Point out each leukocyte.
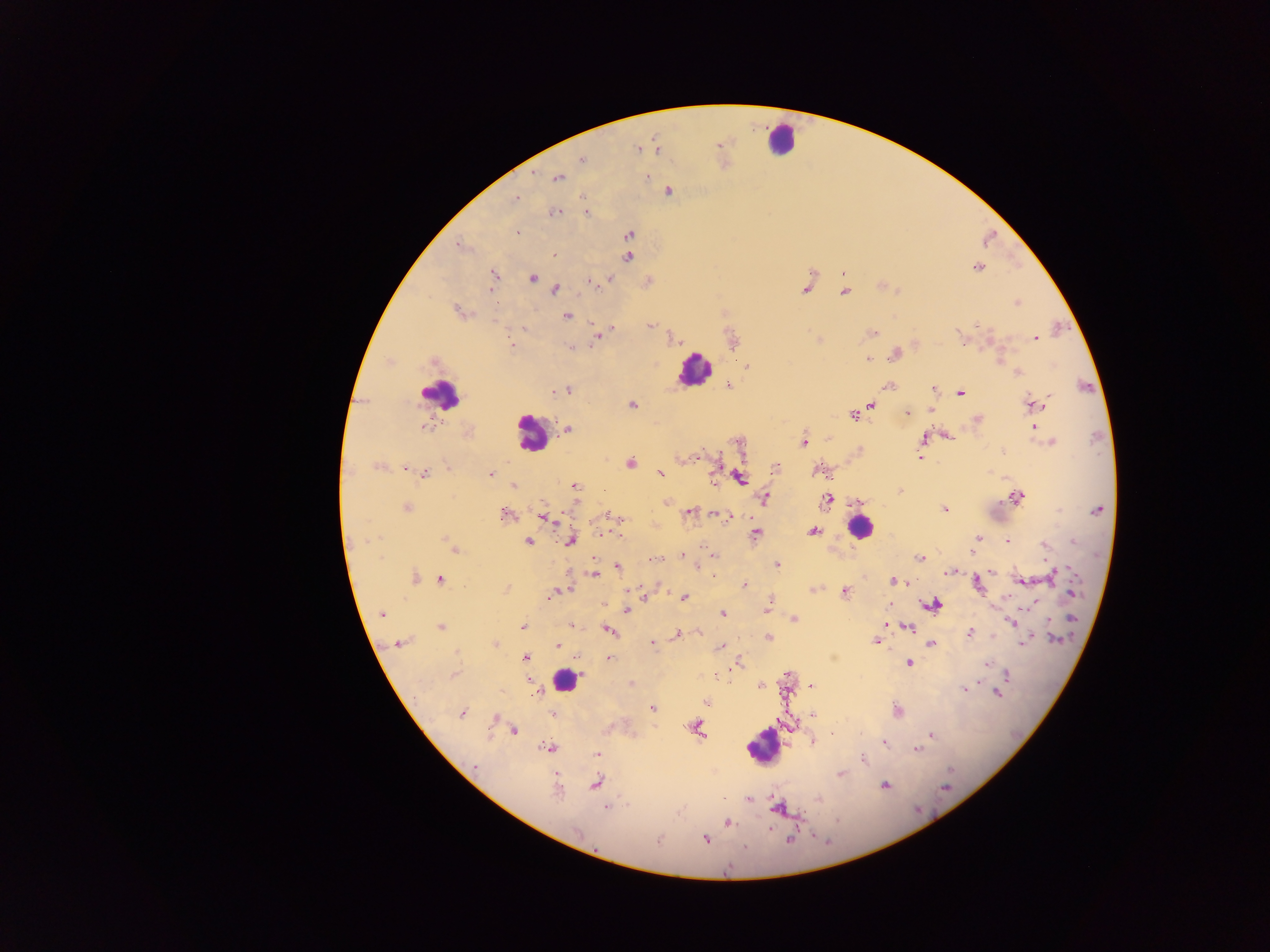

Approximate centers as (x, y) in pixels.
Leukocytes: (780, 139), (695, 371), (441, 395), (531, 433), (859, 527), (564, 676), (762, 746).

Summary:
  - Malaria parasite locations: (638, 149), (657, 149), (582, 160), (646, 176), (557, 177), (668, 191), (516, 198), (554, 212), (586, 212), (517, 232), (629, 234), (459, 246), (554, 256), (628, 257), (978, 267), (844, 273), (494, 275), (532, 278), (608, 279), (594, 282), (555, 289), (806, 289), (490, 290), (845, 292), (1017, 303), (457, 312), (567, 316), (593, 322), (650, 325), (978, 325), (611, 328), (524, 329), (873, 332), (959, 334), (596, 338), (674, 338), (1034, 339), (510, 345), (570, 348), (894, 355), (867, 359), (747, 366), (1018, 373), (728, 386), (888, 387), (934, 389), (567, 390), (556, 391), (960, 393), (872, 404), (1033, 404), (632, 405), (930, 410), (906, 412), (853, 415), (977, 420), (1034, 426), (424, 427), (568, 429), (947, 436), (922, 438), (739, 442), (803, 442), (1051, 442), (1002, 452), (696, 456), (920, 457), (632, 463), (378, 466), (776, 468), (405, 469), (660, 473), (423, 474), (490, 474), (739, 477), (713, 482), (574, 485), (513, 486), (900, 491), (1017, 498), (764, 499), (827, 500), (858, 501), (667, 502), (542, 506), (407, 508), (945, 509), (1097, 510), (690, 513), (505, 515), (606, 515), (718, 515), (543, 516), (727, 517), (619, 518), (812, 531), (756, 533), (977, 539), (570, 541), (1007, 541), (528, 542), (1074, 542), (451, 545), (1044, 546), (454, 548), (973, 551), (681, 554), (715, 556), (920, 557), (652, 560), (777, 565), (618, 566), (948, 572), (991, 572), (595, 574), (1055, 574), (415, 578), (441, 580), (893, 581), (1022, 581), (904, 582), (744, 584), (978, 584), (506, 589), (564, 591), (845, 591), (1071, 592), (552, 594), (645, 597), (684, 598), (602, 604), (890, 604), (933, 604), (627, 610), (766, 611), (382, 614), (723, 614), (1072, 618), (794, 619), (1011, 621), (886, 623), (570, 625), (523, 626), (441, 627), (909, 627), (608, 630), (969, 633), (677, 634), (768, 638), (1056, 640), (876, 641), (1024, 642), (401, 643), (495, 644), (653, 644), (932, 644), (558, 647), (721, 647), (456, 652), (525, 658), (609, 658), (739, 663), (908, 663), (987, 664), (1007, 673), (454, 675), (527, 680), (632, 684), (810, 685), (760, 686), (965, 688), (535, 694), (997, 694), (707, 702), (652, 708), (897, 711), (462, 713), (553, 713), (812, 714), (695, 727), (513, 730), (831, 735), (932, 735), (814, 742), (884, 744), (548, 748), (917, 750), (598, 754), (863, 759), (474, 767), (840, 775), (596, 783), (884, 785), (945, 787), (558, 791), (724, 799), (750, 799), (819, 800), (776, 806), (607, 808), (728, 823), (706, 839), (789, 839), (658, 841), (745, 848)
  - Country: Ghana
  - Capture: mobile-phone photograph through a microscope
  - Field of view: single
  - Image size: 1270×952 pixels
  - Preparation: thick blood smear